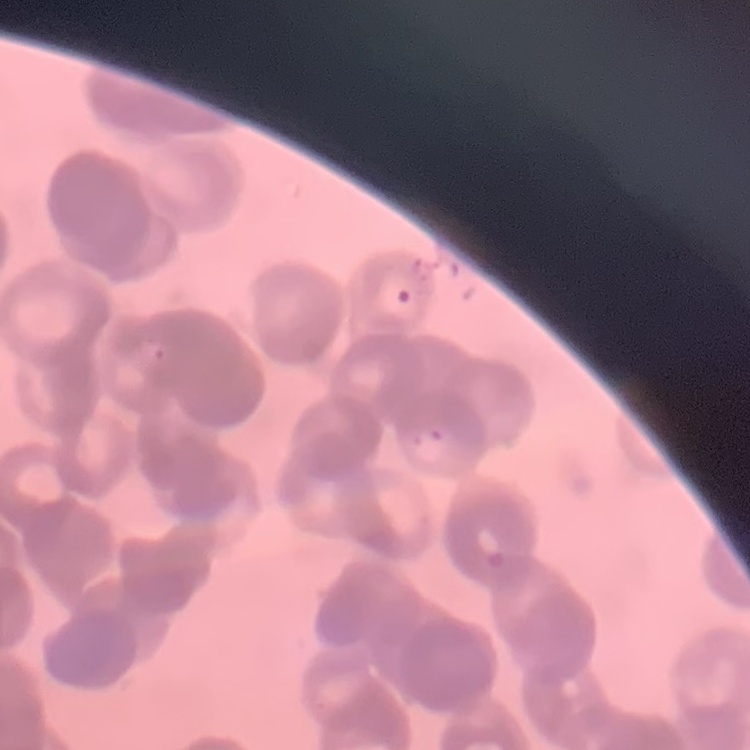
The erythrocytes show rouleaux formation. Thin blood film. Stained with either Field's or Giemsa. Square crop of a larger photomicrograph.